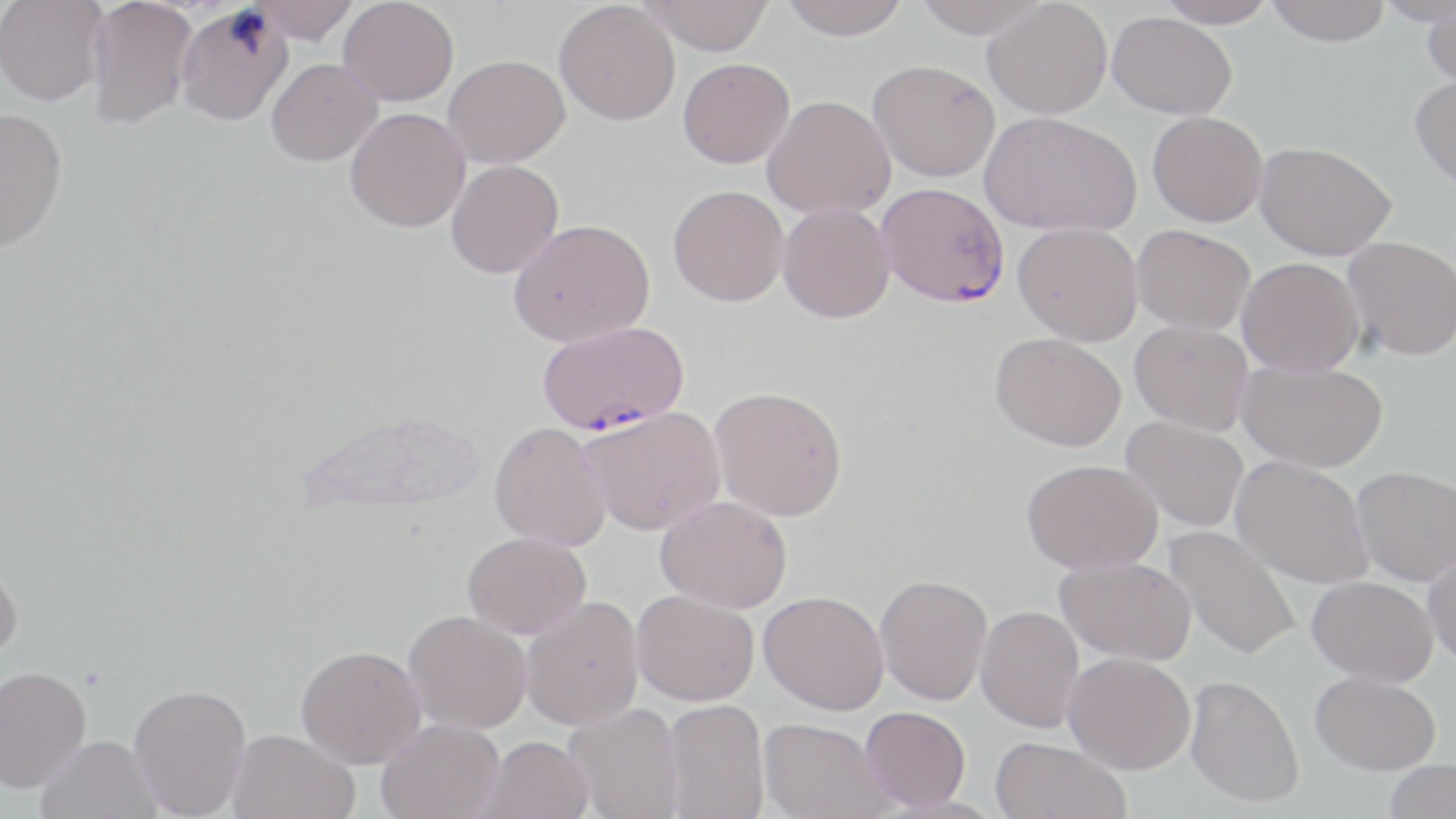
Approximate bounding boxes as named x1/y1/x2/y2 corners in pixels. Plasmodium falciparum-infected red blood cell locations: (x1=876, y1=182, x2=1009, y2=307), (x1=537, y1=321, x2=689, y2=435). Uninfected red blood cell locations: (x1=0, y1=0, x2=108, y2=106), (x1=86, y1=0, x2=197, y2=129), (x1=253, y1=0, x2=359, y2=44), (x1=338, y1=0, x2=459, y2=106), (x1=637, y1=0, x2=774, y2=56), (x1=778, y1=0, x2=910, y2=40), (x1=911, y1=0, x2=1051, y2=39), (x1=983, y1=0, x2=1112, y2=119), (x1=1156, y1=0, x2=1279, y2=28), (x1=1265, y1=0, x2=1391, y2=47), (x1=1375, y1=0, x2=1455, y2=26), (x1=554, y1=1, x2=680, y2=126), (x1=175, y1=4, x2=293, y2=125), (x1=1421, y1=5, x2=1456, y2=90), (x1=1107, y1=12, x2=1237, y2=119), (x1=444, y1=55, x2=570, y2=168), (x1=266, y1=58, x2=382, y2=166), (x1=677, y1=58, x2=795, y2=168), (x1=868, y1=60, x2=1001, y2=182), (x1=1409, y1=73, x2=1456, y2=191), (x1=762, y1=95, x2=896, y2=220), (x1=0, y1=107, x2=68, y2=252), (x1=344, y1=107, x2=470, y2=233), (x1=979, y1=111, x2=1141, y2=237), (x1=1147, y1=111, x2=1268, y2=227), (x1=1254, y1=141, x2=1396, y2=261), (x1=446, y1=159, x2=564, y2=279), (x1=667, y1=185, x2=789, y2=307), (x1=777, y1=203, x2=895, y2=324), (x1=508, y1=218, x2=655, y2=347), (x1=1013, y1=222, x2=1143, y2=346), (x1=1131, y1=224, x2=1256, y2=335), (x1=1343, y1=236, x2=1456, y2=361), (x1=1236, y1=257, x2=1365, y2=376), (x1=1129, y1=320, x2=1254, y2=435), (x1=990, y1=332, x2=1126, y2=451), (x1=1236, y1=359, x2=1388, y2=473), (x1=709, y1=385, x2=848, y2=521), (x1=579, y1=405, x2=726, y2=536), (x1=1121, y1=415, x2=1248, y2=533), (x1=488, y1=421, x2=611, y2=552), (x1=1231, y1=456, x2=1373, y2=589), (x1=1022, y1=459, x2=1162, y2=574), (x1=1351, y1=466, x2=1456, y2=586), (x1=655, y1=495, x2=793, y2=613), (x1=1164, y1=525, x2=1302, y2=661), (x1=462, y1=531, x2=591, y2=638), (x1=1423, y1=547, x2=1456, y2=668), (x1=1055, y1=555, x2=1196, y2=665), (x1=0, y1=556, x2=23, y2=663), (x1=874, y1=574, x2=993, y2=705), (x1=1307, y1=576, x2=1438, y2=685), (x1=631, y1=589, x2=760, y2=706), (x1=758, y1=590, x2=889, y2=715), (x1=520, y1=595, x2=645, y2=731), (x1=975, y1=605, x2=1085, y2=733), (x1=402, y1=610, x2=532, y2=735), (x1=295, y1=645, x2=425, y2=769), (x1=1063, y1=651, x2=1195, y2=775), (x1=0, y1=665, x2=91, y2=793), (x1=1310, y1=671, x2=1441, y2=775), (x1=1185, y1=674, x2=1304, y2=807), (x1=128, y1=683, x2=251, y2=818), (x1=662, y1=698, x2=769, y2=819), (x1=564, y1=702, x2=685, y2=819), (x1=859, y1=706, x2=971, y2=811), (x1=758, y1=717, x2=893, y2=819), (x1=377, y1=718, x2=505, y2=819), (x1=226, y1=729, x2=360, y2=819), (x1=36, y1=734, x2=162, y2=819), (x1=475, y1=735, x2=593, y2=819), (x1=989, y1=736, x2=1131, y2=819), (x1=1383, y1=759, x2=1456, y2=819). Slide-level diagnosis: Plasmodium falciparum. 1000x magnification. Light microscopy. Image is 1456×819 pixels. May-Grünwald-Giemsa stain. Single field of view. Thin blood film.